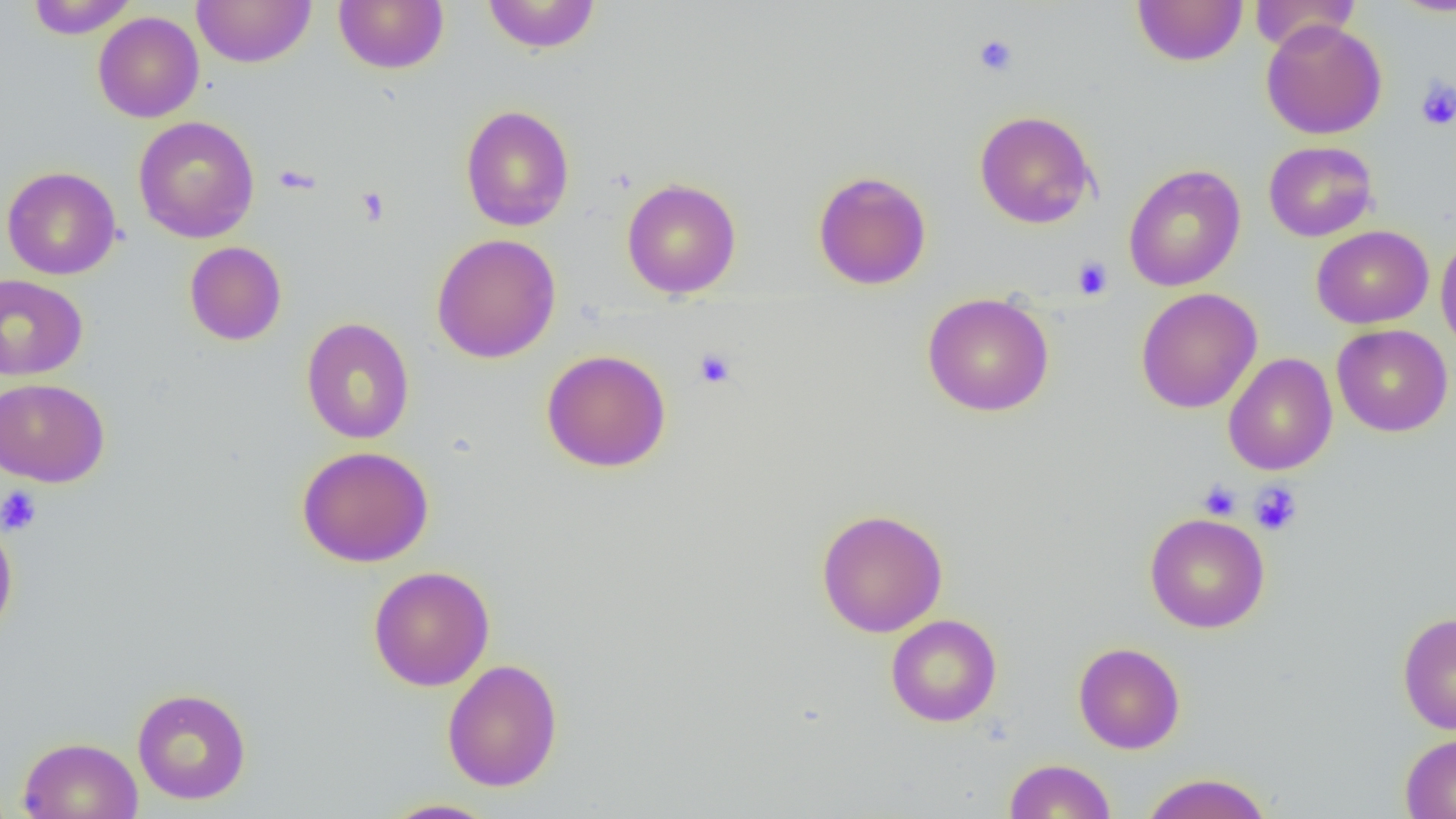

Approximate bounding boxes as [x1, y1, x2, y2] in pixels. Uninfected red blood cell locations: [27, 0, 137, 38], [192, 0, 316, 68], [333, 0, 449, 74], [482, 0, 601, 54], [1249, 0, 1361, 52], [1387, 0, 1456, 16], [1132, 1, 1248, 66], [93, 11, 204, 123], [1261, 19, 1386, 140], [460, 104, 575, 232], [974, 110, 1097, 229], [133, 116, 259, 243], [1263, 141, 1378, 242], [1123, 163, 1246, 292], [2, 166, 121, 280], [813, 170, 932, 290], [622, 178, 741, 298], [1312, 225, 1434, 329], [431, 233, 561, 364], [1435, 233, 1456, 356], [185, 241, 287, 346], [0, 274, 88, 381], [1135, 287, 1263, 413], [922, 292, 1054, 416], [300, 317, 414, 444], [1332, 324, 1453, 437], [541, 349, 672, 472], [1223, 353, 1338, 476], [0, 378, 109, 487], [297, 445, 434, 567], [815, 508, 948, 638], [1144, 512, 1270, 633], [0, 514, 18, 642], [368, 565, 495, 691], [1397, 611, 1456, 735], [886, 614, 1002, 727], [1073, 642, 1185, 754], [442, 658, 563, 791], [132, 687, 252, 805], [1399, 732, 1456, 819], [18, 736, 143, 819], [1003, 758, 1117, 818], [1140, 772, 1273, 819], [381, 798, 501, 818]. Platelet locations: [973, 33, 1018, 77], [1415, 77, 1456, 132], [355, 187, 390, 226], [1072, 256, 1113, 300], [694, 348, 737, 389], [1197, 480, 1241, 520], [1249, 481, 1302, 536], [0, 485, 43, 536]. Slide-level diagnosis: no evidence of blood parasites. 1000x magnification. Single field of view. Optical microscopy. Thin blood smear. Image is 1456×819 pixels.